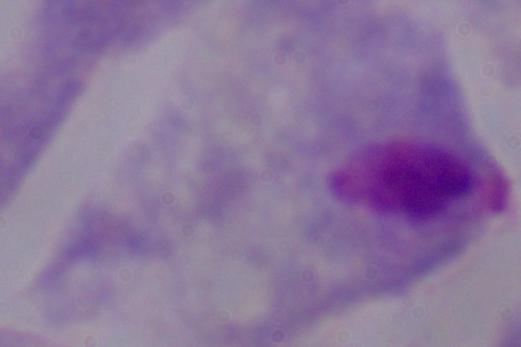
Summary:
  - Modality: photomicrograph
  - Magnification: 1000x
  - Identification: trichomonad